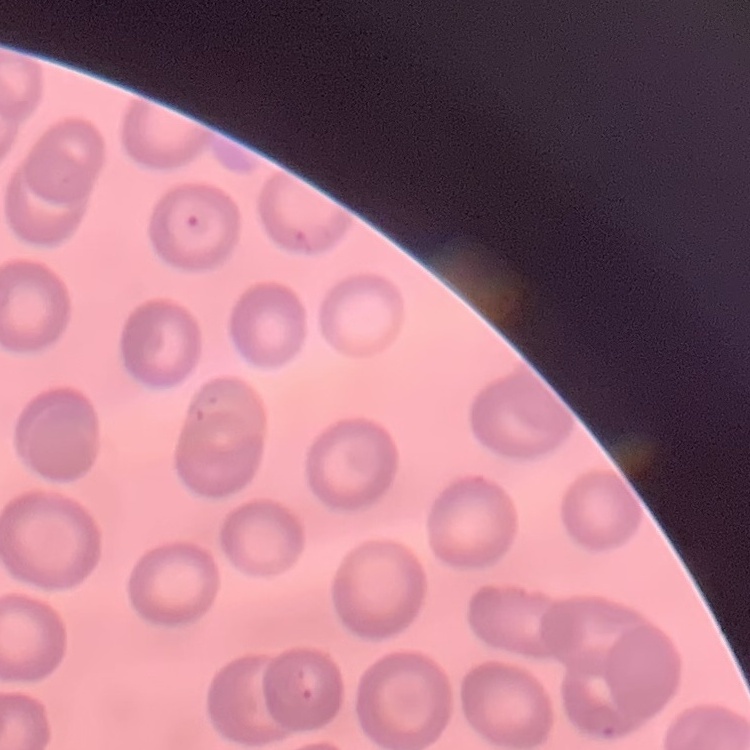

The erythrocytes show no rouleaux formation. Thin blood film. Field's or Giemsa stain. Square crop of a larger photomicrograph.